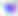
Micrograph. Toxoplasma gondii is shown. Captured at 400x magnification.